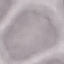

Result: no malaria parasites detected. Thin blood film. Photographed with a smartphone camera at the microscope eyepiece. Giemsa stain. Cell patch, automatically extracted from a larger field of view and resized to 64 × 64 pixels.